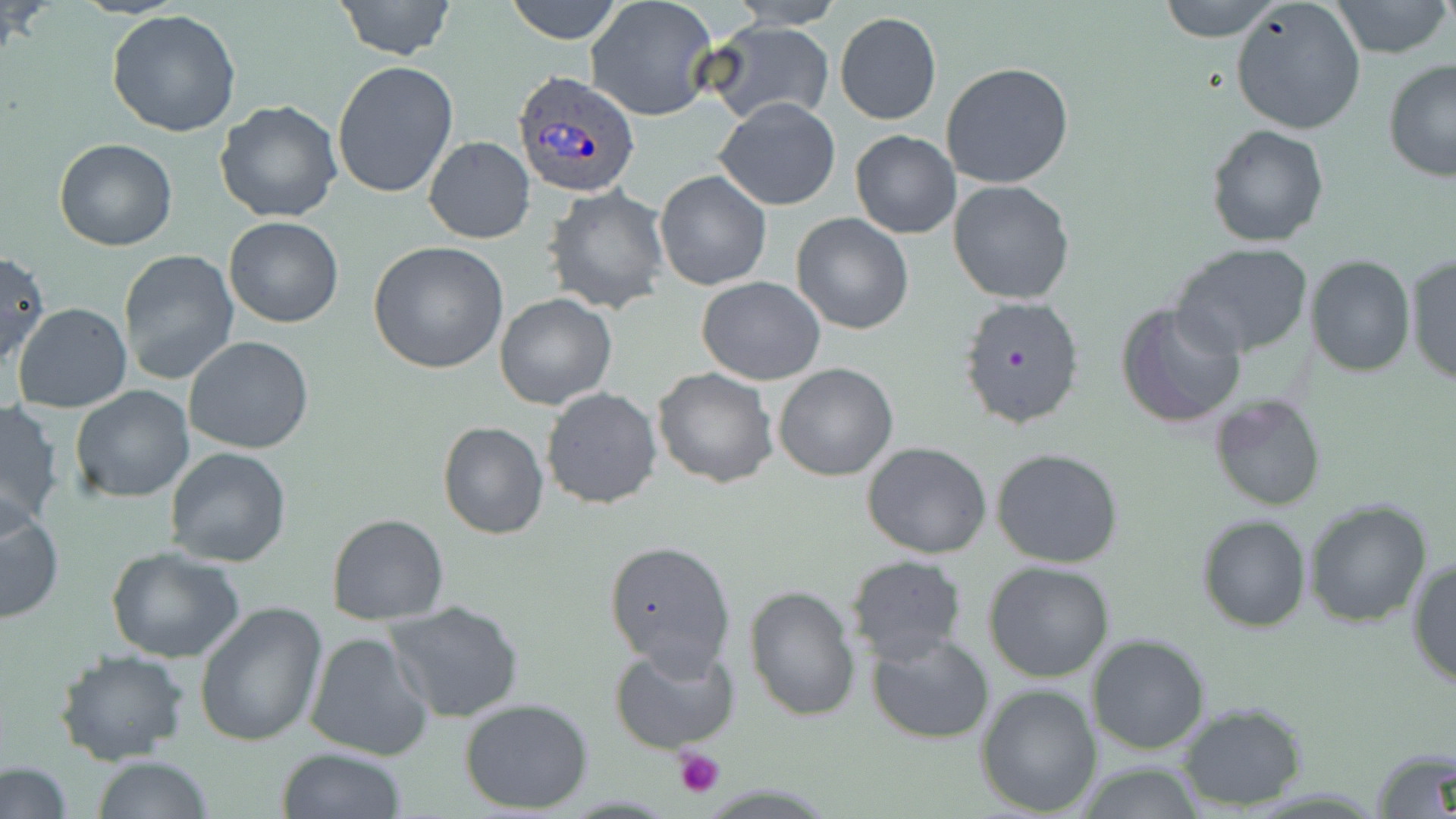 Approximate bounding boxes as (x1, y1, x2, y2) in pixels. Platelet locations: (673, 748, 726, 797). Plasmodium ovale-infected red blood cell locations: (511, 70, 639, 198). Uninfected red blood cell locations: (331, 0, 458, 60), (504, 0, 624, 44), (724, 0, 850, 28), (1156, 0, 1283, 42), (1328, 0, 1455, 60), (586, 1, 718, 121), (1229, 1, 1366, 136), (105, 9, 244, 138), (835, 11, 942, 125), (703, 20, 834, 127), (332, 60, 458, 199), (1382, 60, 1456, 183), (941, 62, 1076, 189), (714, 97, 841, 211), (214, 100, 344, 223), (1205, 124, 1329, 247), (851, 130, 960, 239), (424, 137, 535, 243), (55, 139, 178, 252), (655, 170, 771, 290), (948, 180, 1075, 303), (543, 185, 669, 313), (791, 213, 913, 334), (224, 216, 344, 328), (368, 241, 511, 374), (1168, 243, 1314, 358), (117, 248, 240, 386), (0, 251, 49, 367), (1405, 252, 1455, 385), (1306, 255, 1414, 376), (1137, 265, 1280, 402), (696, 277, 825, 386), (494, 293, 617, 409), (956, 294, 1086, 433), (1116, 299, 1246, 430), (12, 302, 132, 413), (184, 336, 315, 455), (773, 364, 898, 481), (652, 367, 779, 488), (70, 384, 196, 504), (541, 386, 662, 509), (1208, 393, 1326, 512), (0, 398, 66, 531), (437, 421, 549, 539), (862, 441, 992, 560), (164, 447, 292, 567), (992, 448, 1124, 569), (1304, 498, 1433, 628), (0, 499, 65, 625), (327, 513, 449, 624), (1197, 514, 1312, 633), (602, 539, 736, 671), (105, 547, 245, 663), (844, 554, 968, 665), (1408, 554, 1456, 691), (982, 559, 1116, 682), (745, 585, 861, 723), (195, 600, 329, 747), (384, 600, 525, 723), (302, 630, 435, 761), (865, 631, 995, 743), (1088, 634, 1212, 755), (610, 638, 739, 753), (54, 649, 190, 767), (976, 681, 1103, 816), (459, 697, 595, 814), (1175, 702, 1310, 809), (1371, 745, 1456, 818), (277, 747, 406, 819), (91, 755, 215, 818), (2, 762, 73, 817), (1071, 762, 1210, 817). Slide-level diagnosis: Plasmodium ovale. May-Grünwald-Giemsa stain. Image is 1456×819 pixels. Light microscopy. Captured at 1000x magnification. Single field of view. Thin blood film.